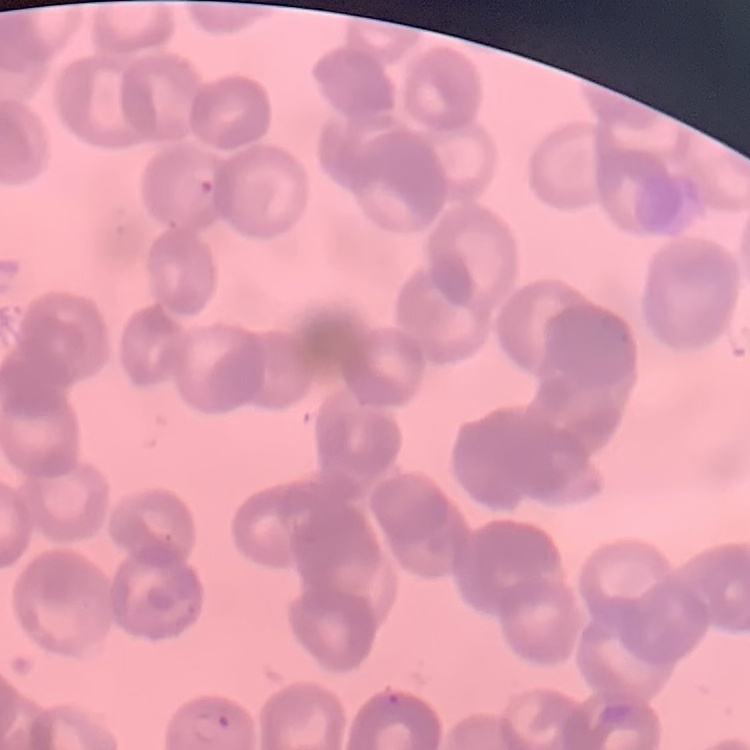

red blood cell morphology = rouleaux formation
image type = square crop of a larger photomicrograph
stain = Field's or Giemsa
preparation = thin blood smear